Give the extent of all uninfected red blood cells.
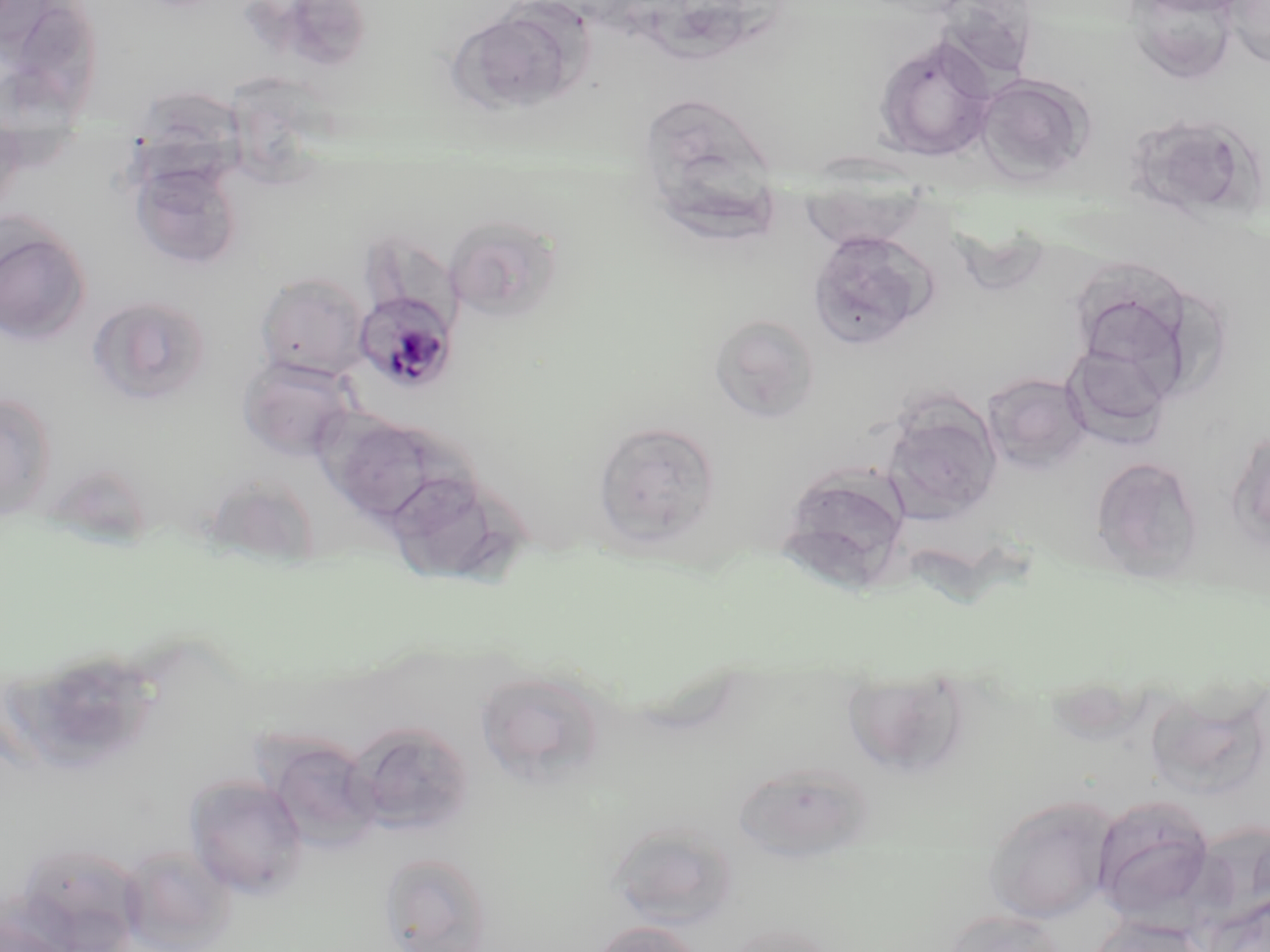

Approximate bounding boxes as [x1, y1, x2, y2] in pixels.
Uninfected red blood cells: [1222, 0, 1270, 68], [1124, 1, 1243, 82], [237, 2, 377, 78], [448, 5, 587, 115], [16, 11, 106, 163], [872, 33, 999, 162], [976, 72, 1094, 185], [228, 75, 358, 189], [126, 88, 255, 200], [644, 104, 785, 255], [1126, 110, 1259, 221], [0, 120, 27, 218], [807, 155, 928, 247], [129, 157, 245, 270], [443, 214, 564, 324], [0, 218, 92, 347], [806, 229, 936, 351], [357, 230, 460, 330], [1066, 260, 1202, 393], [256, 272, 372, 380], [86, 294, 213, 407], [708, 314, 821, 423], [1062, 342, 1174, 448], [239, 355, 357, 461], [981, 371, 1091, 473], [0, 392, 58, 521], [882, 398, 1002, 522], [330, 415, 443, 523], [592, 420, 722, 549], [1228, 428, 1270, 549], [1091, 456, 1204, 579], [777, 464, 913, 593], [54, 470, 153, 565], [386, 471, 526, 587], [202, 475, 322, 570], [30, 646, 165, 771], [474, 668, 607, 789], [856, 668, 968, 774], [1151, 680, 1260, 797], [348, 721, 475, 837], [263, 735, 384, 854], [732, 760, 876, 863], [185, 774, 309, 899], [982, 793, 1120, 925], [1091, 794, 1217, 924], [606, 821, 740, 929], [15, 843, 144, 949], [120, 844, 236, 952], [378, 851, 494, 952], [1203, 891, 1270, 952], [0, 907, 77, 952], [942, 908, 1068, 952], [1086, 916, 1212, 952], [590, 920, 703, 952], [718, 920, 840, 952].

Plasmodium malariae-infected red blood cell locations: [355, 292, 457, 394]. Slide-level diagnosis: Plasmodium malariae. Captured at 1000x magnification. One field of a larger specimen. Optical microscopy. Thin blood smear. Image is 1270×952 pixels. May-Grünwald-Giemsa-stained preparation.